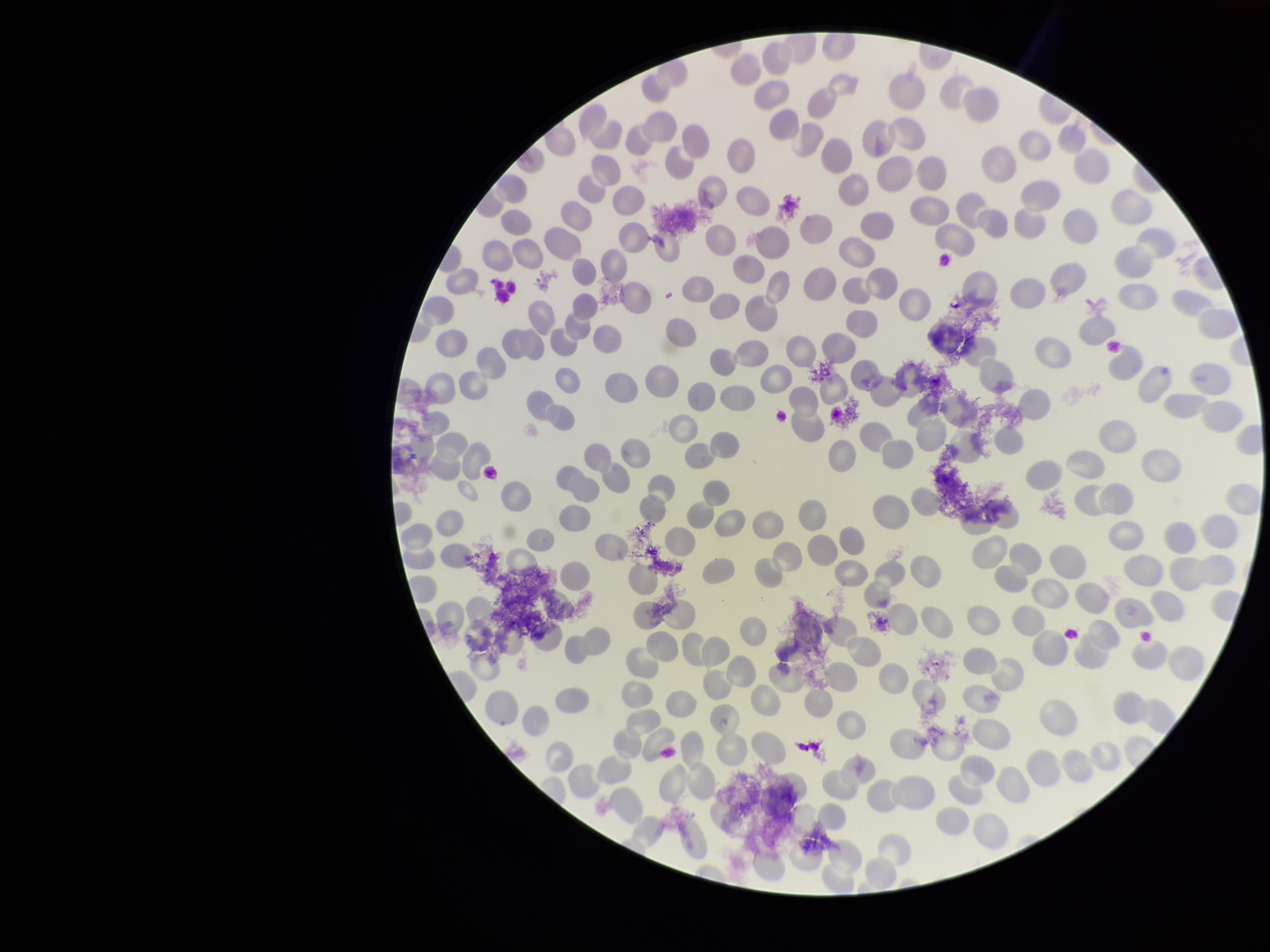

Red blood cell count: 238. Parasitized red blood cells: none identified. Single field of view. Stained with Giemsa. Image is 1270×952 pixels. Preparation: thin smear. Parasitized red blood cell count: 0. Photographed through the microscope eyepiece with a smartphone camera. Patient malaria status: negative.